Evaluate for malaria.
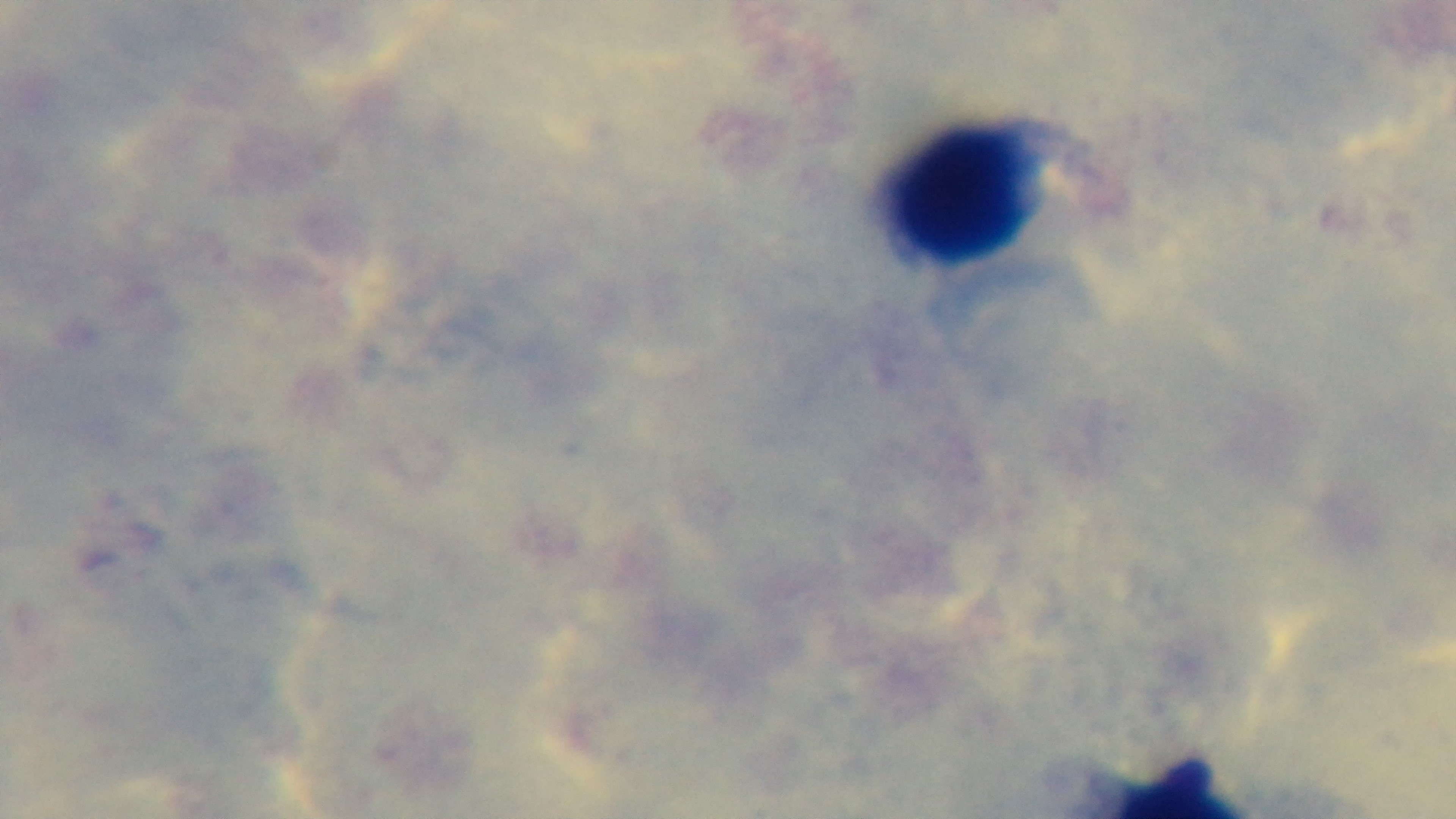

It is uninfected.

Summary:
  - Field of view: one from the slide
  - Modality: light microscopy
  - Capture: mounted 4K digital camera
  - Stain: Giemsa
  - Preparation: thick
  - Objective: 100x oil immersion